State which parasite is depicted.
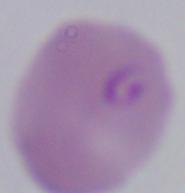
Babesia.

1000x magnification. Micrograph.